Report the malaria status of this cell.
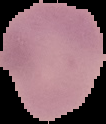
Parasitized.

{
  "image_size": "106×124 pixels",
  "image_type": "segmented cell region with the area outside set to black",
  "preparation": "thin blood film"
}